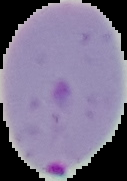
result: Plasmodium parasites detected
image_size: 127×181 pixels
image_type: segmented cell region on a black background
preparation: thin blood film